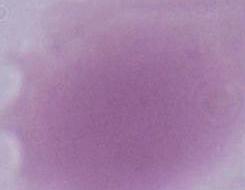
{
  "magnification": "1000x",
  "modality": "micrograph",
  "identification": "erythrocyte"
}